Comment on the morphology of the red blood cells.
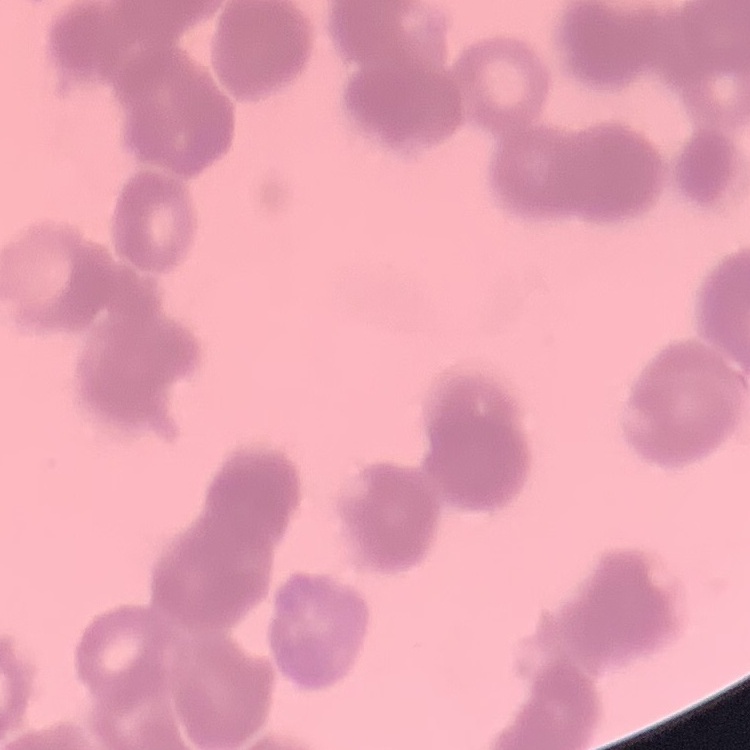

Rouleaux formation.

Stained with either Field's or Giemsa. Thin blood smear. Square crop of a larger photomicrograph.